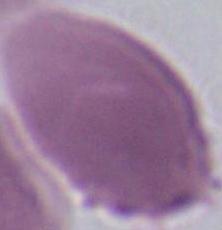 1000x magnification. A red blood cell is shown. Micrograph.